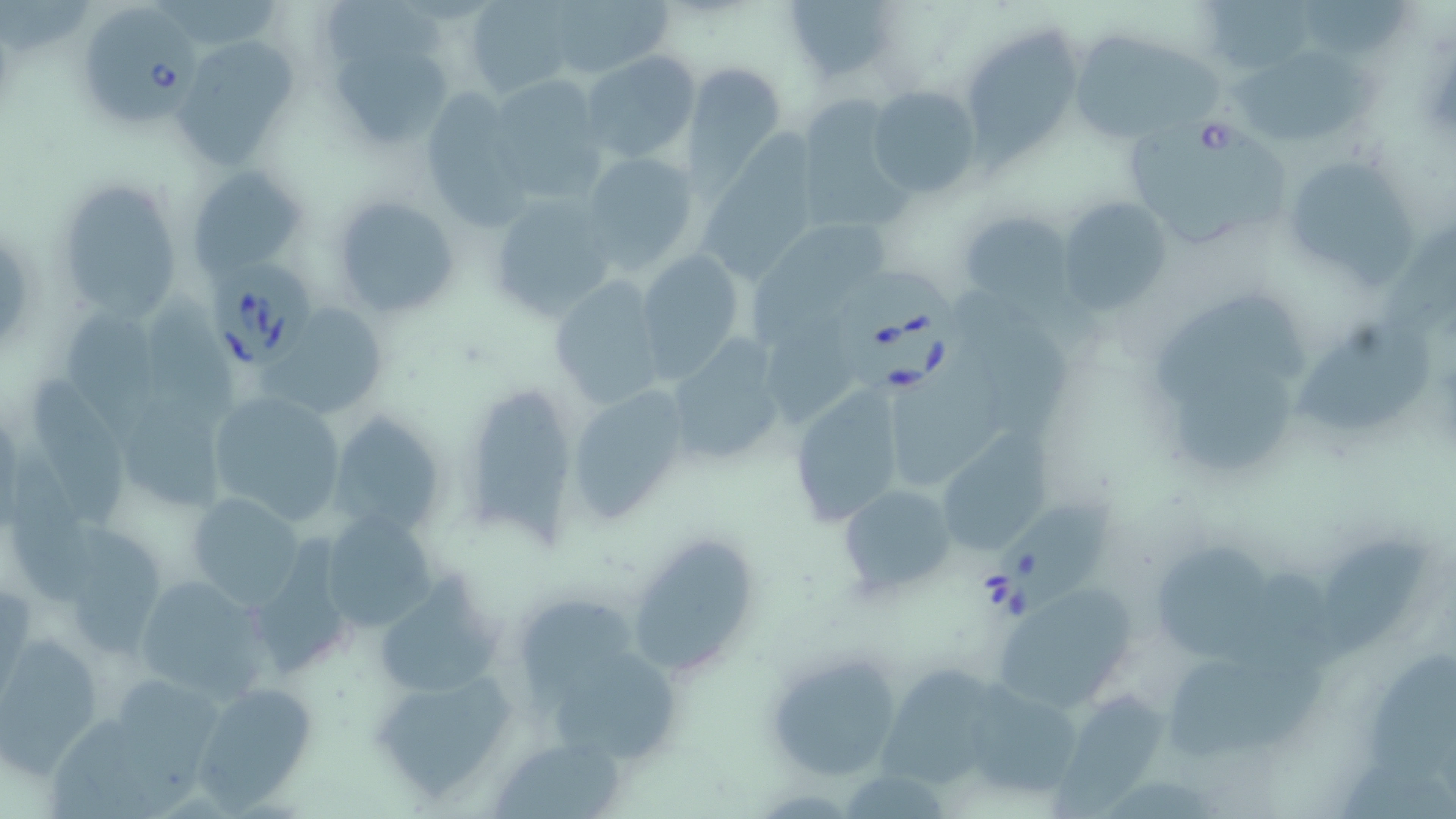
slide-level diagnosis = Babesia divergens
preparation = thin blood smear
uninfected red blood cell locations = approximate bounding boxes as (x1,y1)-(x2,y2) corner pairs in pixels: (784,0)-(901,82), (543,1)-(672,81), (467,2)-(575,97), (973,28)-(1081,166), (176,33)-(302,167), (1068,35)-(1232,138), (329,39)-(448,151), (582,50)-(701,163), (1236,56)-(1381,145), (685,63)-(784,178), (869,85)-(981,198), (803,99)-(917,227), (700,119)-(828,290), (579,151)-(700,273), (1288,161)-(1422,294), (187,165)-(306,278), (55,176)-(188,324), (487,191)-(617,321), (331,195)-(459,318), (1058,195)-(1172,314), (960,211)-(1070,306), (747,216)-(887,355), (634,250)-(745,381), (548,275)-(666,413), (1149,291)-(1303,393), (153,295)-(241,422), (264,302)-(386,419), (64,310)-(173,446), (1290,316)-(1436,433), (665,337)-(784,468), (1178,356)-(1304,476), (890,362)-(1012,485), (35,377)-(125,532), (467,383)-(576,552), (568,385)-(691,523), (788,386)-(905,527), (207,393)-(348,525), (125,395)-(231,513), (326,411)-(449,537), (952,426)-(1056,548), (8,453)-(105,605), (836,484)-(957,597), (186,492)-(307,609), (311,508)-(443,637), (70,529)-(166,650), (625,529)-(760,679), (1322,529)-(1429,664), (1140,539)-(1282,660), (251,541)-(355,670), (378,568)-(517,696), (131,573)-(272,703), (991,585)-(1140,712), (523,598)-(642,706), (0,632)-(107,773), (762,648)-(903,782), (1169,653)-(1326,763), (556,654)-(682,768), (1366,657)-(1456,780), (866,659)-(1009,792), (366,668)-(520,805), (190,682)-(321,810), (968,688)-(1087,795), (1052,690)-(1176,819), (492,735)-(626,818)
modality = light microscopy
Babesia divergens-infected red blood cell locations = approximate bounding boxes as (x1,y1)-(x2,y2) corner pairs in pixels: (86,3)-(199,127), (1129,115)-(1296,253), (211,258)-(316,368), (831,262)-(963,397), (981,491)-(1119,626)
field of view = one of a larger specimen
magnification = 1000x
image size = 1456×819 pixels
stain = May-Grünwald-Giemsa